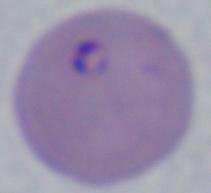

Summary:
  - Magnification: 1000x
  - Identification: Babesia
  - Modality: photomicrograph